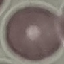 Malaria status: uninfected. Thin smear of blood. Cell patch, automatically extracted from a larger field of view and resized to 64 × 64 pixels. Photographed with a smartphone camera at the microscope eyepiece. Giemsa-stained preparation.